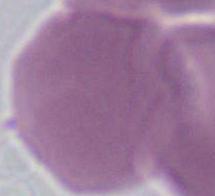

modality = micrograph
identification = erythrocyte
magnification = 1000x